Locate every Babesia divergens-infected red blood cell.
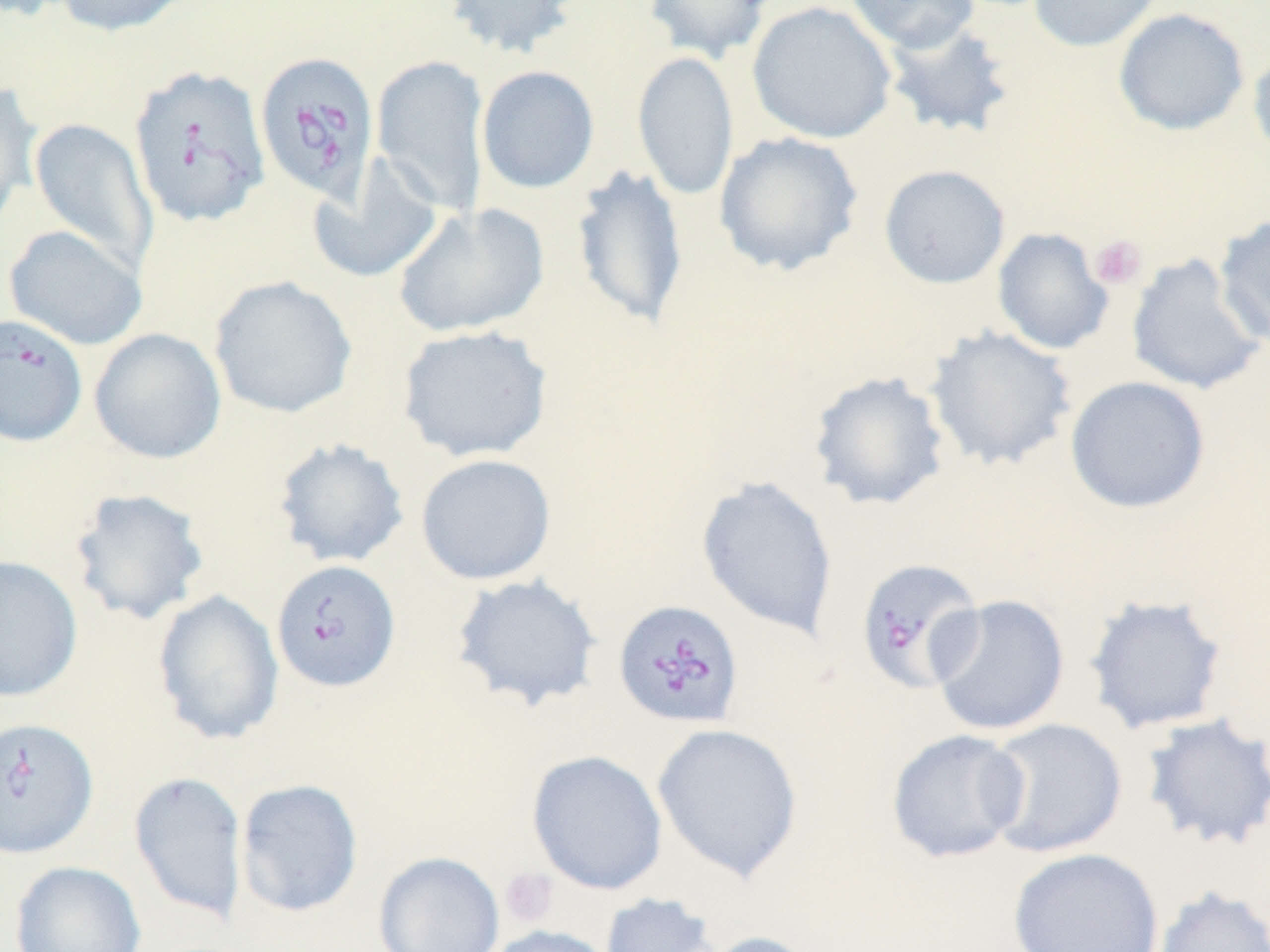
Approximate bounding boxes as (x1, y1, x2, y2) in pixels.
Babesia divergens-infected red blood cells: (254, 51, 380, 204), (127, 64, 272, 229), (0, 313, 88, 448), (854, 557, 986, 694), (271, 559, 401, 693), (613, 599, 745, 729), (1, 715, 99, 859).

Summary:
  - Platelet locations: (1089, 234, 1148, 290), (500, 867, 559, 926)
  - Uninfected red blood cell locations: (53, 0, 194, 37), (443, 0, 579, 59), (643, 0, 774, 63), (846, 0, 981, 53), (1028, 0, 1165, 53), (747, 1, 897, 144), (1112, 8, 1250, 136), (879, 19, 1017, 141), (1247, 43, 1270, 166), (632, 50, 738, 201), (371, 53, 490, 215), (476, 65, 600, 194), (0, 81, 43, 229), (28, 117, 159, 275), (714, 131, 864, 276), (307, 157, 444, 284), (570, 163, 689, 331), (878, 164, 1010, 289), (392, 202, 549, 338), (1214, 213, 1270, 349), (3, 225, 148, 350), (992, 227, 1113, 355), (1126, 252, 1267, 396), (208, 274, 357, 419), (396, 324, 554, 462), (924, 325, 1078, 471), (89, 328, 226, 464), (807, 370, 952, 512), (1065, 375, 1211, 514), (272, 437, 410, 569), (415, 453, 557, 585), (696, 474, 840, 640), (67, 487, 211, 626), (0, 555, 83, 703), (451, 573, 603, 712), (152, 589, 284, 746), (1082, 593, 1229, 734), (928, 594, 1071, 737), (1139, 713, 1270, 853), (982, 717, 1128, 858), (651, 722, 804, 884), (886, 728, 1029, 864), (526, 749, 668, 895), (128, 770, 248, 926), (235, 778, 364, 918), (1007, 847, 1164, 952), (373, 851, 506, 952), (10, 860, 147, 952), (1151, 884, 1270, 952), (599, 891, 722, 952), (484, 925, 615, 952), (700, 930, 822, 952)
  - Slide-level diagnosis: Babesia divergens
  - Field of view: single
  - Modality: optical microscopy
  - Preparation: thin blood smear
  - Stain: May-Grünwald-Giemsa
  - Image size: 1270×952 pixels
  - Magnification: 1000x